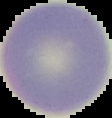

Summary:
  - Image size: 112×118 pixels
  - Preparation: thin blood film
  - Result: no Plasmodium parasites detected
  - Image type: cell region segmented out of the field of view; surrounding area masked to black